State which cell type is depicted.
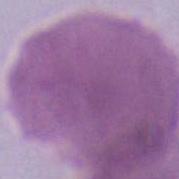

An erythrocyte.

Summary:
  - Magnification: 1000x
  - Modality: photomicrograph